Name the parasite shown.
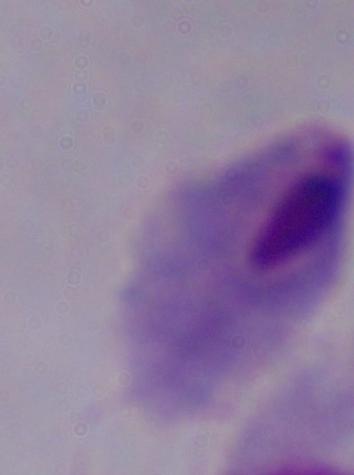
A trichomonad.

Summary:
  - Magnification: 1000x
  - Modality: micrograph